Locate every blood parasite and identify its species.
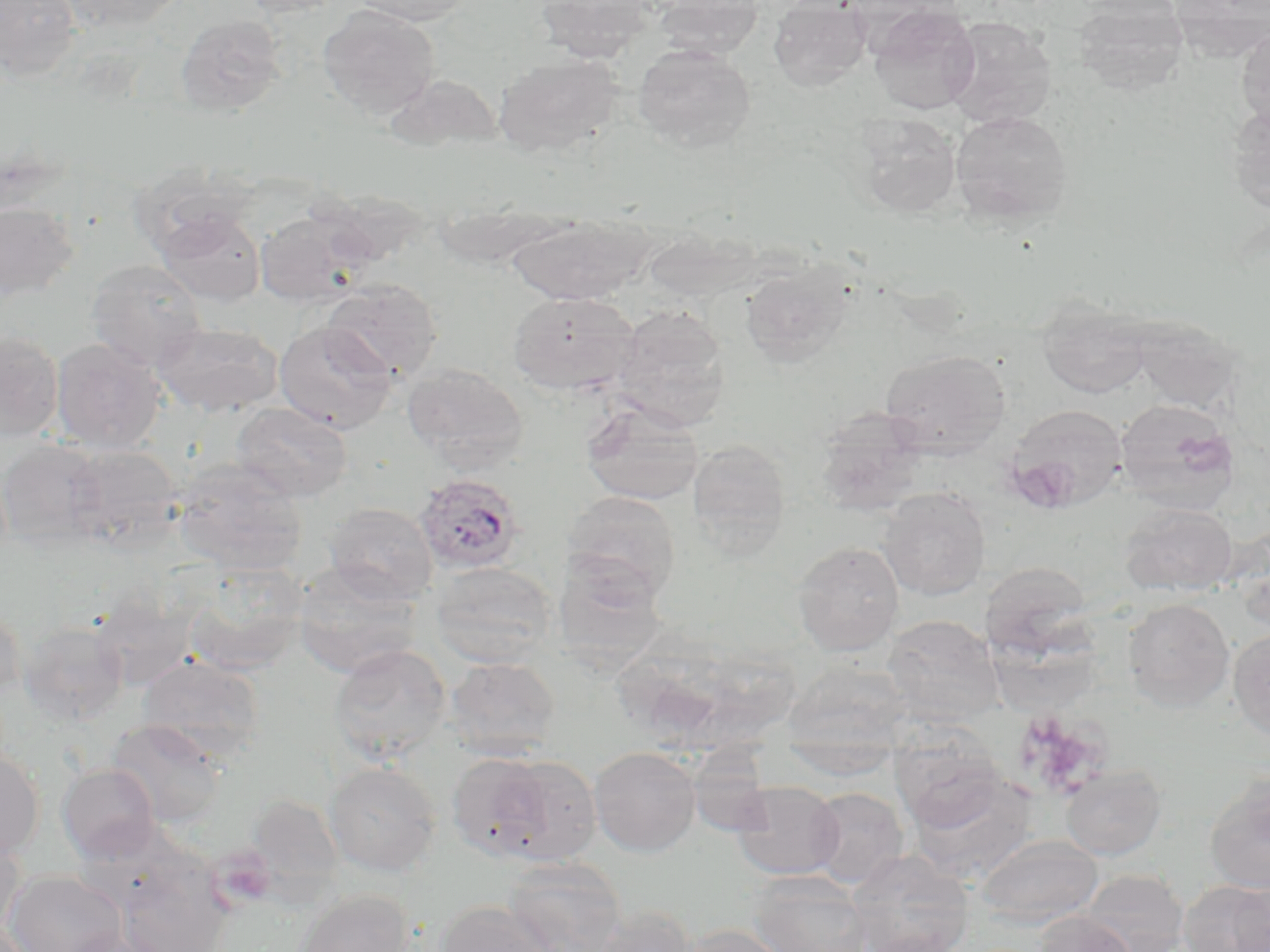

Approximate bounding boxes as named x1/y1/x2/y2 corners in pixels.
Plasmodium ovale-infected red blood cells: (x1=414, y1=472, x2=526, y2=575).
No Plasmodium falciparum, Plasmodium malariae, Plasmodium vivax, Babesia divergens, or Trypanosoma brucei observed.

{
  "slide_level_diagnosis": "Plasmodium ovale",
  "modality": "optical microscopy",
  "uninfected_red_blood_cell_locations": "approximate bounding boxes as named x1/y1/x2/y2 corners in pixels: (x1=0, y1=0, x2=82, y2=81), (x1=58, y1=0, x2=188, y2=32), (x1=239, y1=0, x2=347, y2=17), (x1=350, y1=0, x2=470, y2=26), (x1=536, y1=0, x2=660, y2=62), (x1=654, y1=0, x2=765, y2=58), (x1=768, y1=0, x2=873, y2=90), (x1=1072, y1=2, x2=1190, y2=95), (x1=317, y1=4, x2=440, y2=121), (x1=867, y1=5, x2=981, y2=115), (x1=174, y1=14, x2=287, y2=118), (x1=943, y1=17, x2=1057, y2=129), (x1=1236, y1=27, x2=1270, y2=134), (x1=632, y1=44, x2=756, y2=152), (x1=492, y1=54, x2=623, y2=157), (x1=384, y1=74, x2=503, y2=152), (x1=1225, y1=102, x2=1270, y2=214), (x1=950, y1=109, x2=1072, y2=226), (x1=851, y1=113, x2=961, y2=218), (x1=129, y1=164, x2=255, y2=260), (x1=0, y1=202, x2=79, y2=301), (x1=254, y1=208, x2=372, y2=308), (x1=156, y1=209, x2=266, y2=306), (x1=506, y1=213, x2=654, y2=304), (x1=86, y1=259, x2=207, y2=370), (x1=739, y1=259, x2=857, y2=367), (x1=323, y1=279, x2=442, y2=382), (x1=506, y1=291, x2=639, y2=395), (x1=1037, y1=298, x2=1153, y2=399), (x1=611, y1=304, x2=731, y2=428), (x1=1131, y1=317, x2=1241, y2=414), (x1=274, y1=320, x2=398, y2=434), (x1=154, y1=322, x2=282, y2=417), (x1=0, y1=330, x2=64, y2=441), (x1=51, y1=338, x2=166, y2=453), (x1=881, y1=349, x2=1011, y2=457), (x1=402, y1=363, x2=529, y2=470), (x1=1114, y1=398, x2=1240, y2=514), (x1=580, y1=399, x2=705, y2=506), (x1=230, y1=402, x2=353, y2=503), (x1=1003, y1=405, x2=1128, y2=513), (x1=814, y1=408, x2=928, y2=516), (x1=0, y1=439, x2=107, y2=545), (x1=688, y1=439, x2=791, y2=555), (x1=66, y1=445, x2=184, y2=551), (x1=171, y1=458, x2=308, y2=574), (x1=878, y1=487, x2=990, y2=600), (x1=562, y1=491, x2=681, y2=602), (x1=324, y1=502, x2=437, y2=604), (x1=1119, y1=503, x2=1237, y2=596), (x1=792, y1=540, x2=904, y2=657), (x1=430, y1=561, x2=558, y2=668), (x1=981, y1=561, x2=1094, y2=659), (x1=182, y1=562, x2=307, y2=675), (x1=292, y1=562, x2=424, y2=677), (x1=90, y1=590, x2=201, y2=691), (x1=1123, y1=598, x2=1235, y2=712), (x1=0, y1=602, x2=25, y2=701), (x1=882, y1=614, x2=1003, y2=724), (x1=18, y1=621, x2=128, y2=725), (x1=1228, y1=628, x2=1270, y2=741), (x1=329, y1=644, x2=452, y2=763), (x1=138, y1=655, x2=266, y2=763), (x1=445, y1=657, x2=561, y2=760), (x1=783, y1=661, x2=914, y2=747), (x1=107, y1=718, x2=227, y2=829), (x1=889, y1=734, x2=1005, y2=832), (x1=589, y1=746, x2=702, y2=857), (x1=782, y1=746, x2=898, y2=779), (x1=0, y1=748, x2=44, y2=859), (x1=682, y1=751, x2=778, y2=836), (x1=446, y1=752, x2=558, y2=862), (x1=485, y1=755, x2=602, y2=866), (x1=324, y1=761, x2=441, y2=876), (x1=58, y1=763, x2=159, y2=861), (x1=1060, y1=764, x2=1167, y2=860), (x1=908, y1=769, x2=1038, y2=885), (x1=1203, y1=773, x2=1270, y2=895), (x1=731, y1=781, x2=844, y2=880), (x1=807, y1=787, x2=909, y2=888), (x1=245, y1=793, x2=345, y2=900), (x1=0, y1=830, x2=27, y2=936), (x1=975, y1=834, x2=1103, y2=928), (x1=844, y1=850, x2=974, y2=952), (x1=502, y1=857, x2=627, y2=952), (x1=113, y1=858, x2=233, y2=952), (x1=1080, y1=869, x2=1189, y2=952), (x1=5, y1=870, x2=126, y2=952), (x1=747, y1=870, x2=871, y2=952), (x1=1179, y1=878, x2=1270, y2=951), (x1=296, y1=889, x2=416, y2=952), (x1=435, y1=900, x2=557, y2=952), (x1=591, y1=904, x2=698, y2=952), (x1=1031, y1=911, x2=1139, y2=952), (x1=680, y1=923, x2=792, y2=952), (x1=60, y1=931, x2=169, y2=952)",
  "image_size": "1270×952 pixels",
  "field_of_view": "single",
  "stain": "May-Grünwald-Giemsa",
  "preparation": "thin blood film",
  "magnification": "1000x"
}